Classify this cell by malaria status.
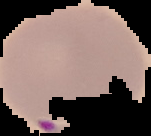
Parasitized.

image_type: segmented cell region on a black background
image_size: 151×136 pixels
preparation: thin blood smear